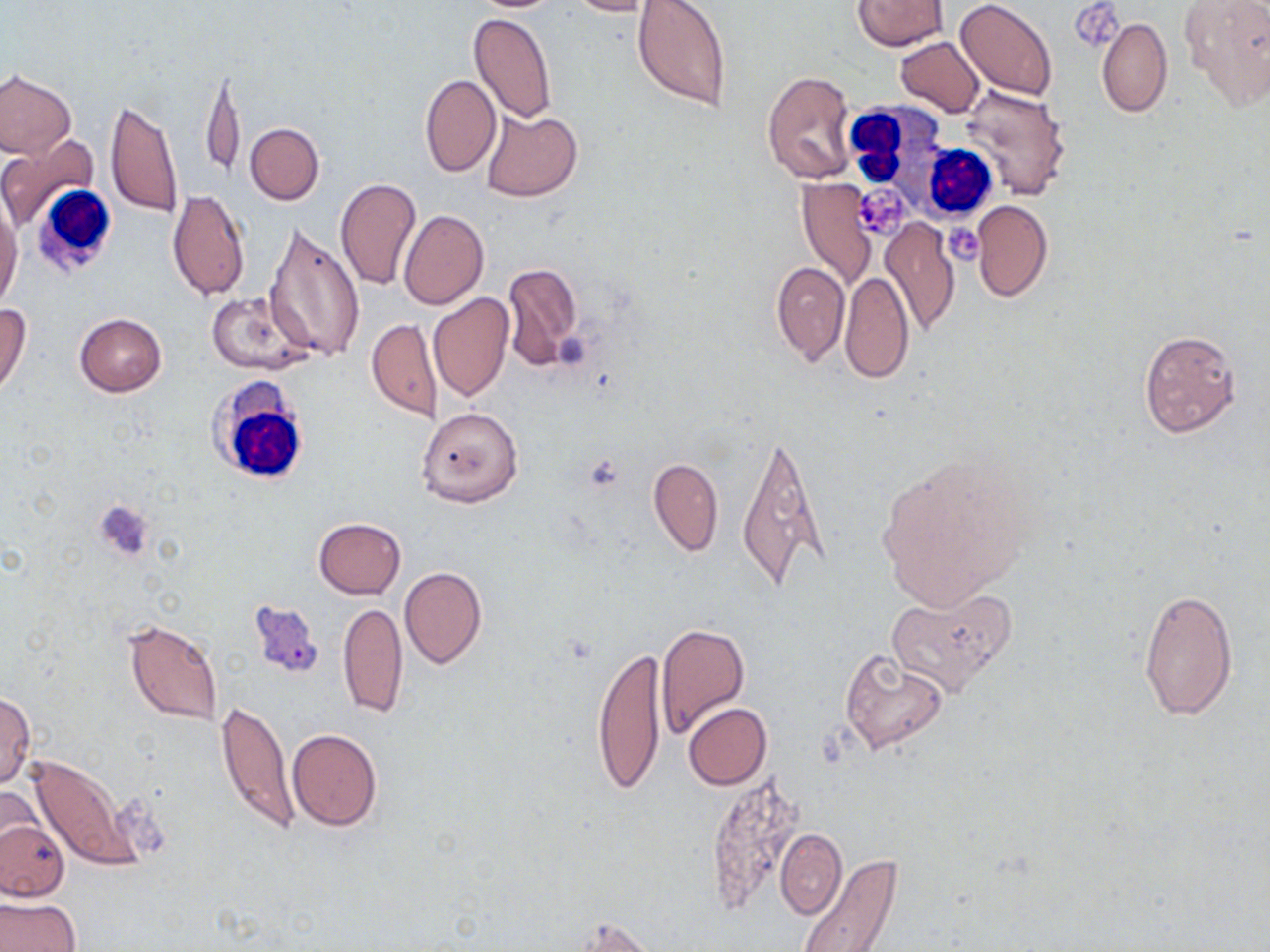
Approximate bounding boxes as (x1, y1, x2, y2) in pixels. White blood cell locations: (847, 100, 936, 192), (909, 144, 1002, 221), (32, 184, 119, 278), (205, 377, 314, 487). Platelet locations: (1072, 2, 1119, 46), (854, 184, 913, 239), (946, 226, 981, 263). Uninfected red blood cell locations: (469, 0, 566, 12), (564, 0, 660, 16), (631, 0, 731, 111), (852, 0, 947, 50), (956, 0, 1058, 103), (1179, 0, 1270, 111), (468, 13, 557, 124), (1098, 19, 1172, 118), (895, 36, 985, 117), (202, 63, 243, 179), (0, 69, 75, 160), (762, 70, 857, 184), (421, 74, 501, 176), (959, 85, 1072, 201), (105, 97, 182, 219), (480, 110, 583, 201), (244, 122, 323, 205), (0, 134, 98, 231), (335, 176, 421, 291), (797, 178, 877, 287), (168, 190, 249, 301), (0, 196, 22, 312), (971, 200, 1052, 303), (399, 209, 488, 309), (880, 219, 961, 335), (262, 220, 365, 363), (772, 261, 849, 365), (500, 264, 583, 372), (840, 271, 915, 385), (207, 292, 315, 376), (428, 292, 513, 403), (0, 303, 31, 398), (74, 312, 168, 397), (367, 318, 442, 421), (1139, 328, 1241, 436), (417, 406, 524, 508), (736, 429, 824, 594), (874, 450, 1036, 612), (648, 457, 723, 555), (313, 518, 406, 599), (399, 566, 488, 669), (885, 586, 1018, 697), (1139, 587, 1238, 719), (338, 601, 408, 718), (122, 618, 225, 727), (655, 619, 750, 737), (592, 643, 666, 797), (838, 649, 950, 756), (0, 690, 36, 788), (217, 700, 298, 834), (683, 703, 772, 789), (286, 728, 383, 831), (27, 752, 146, 873), (704, 779, 809, 898), (0, 783, 44, 866), (0, 817, 69, 902), (774, 829, 846, 919), (799, 852, 905, 952), (0, 895, 81, 952), (566, 914, 658, 951). Slide-level diagnosis: no evidence of blood parasites. 1000x magnification. Thin blood smear. May-Grünwald-Giemsa stain. Optical microscopy. Single field of view. Image is 1270×952 pixels.